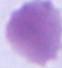

magnification: 1000x
modality: photomicrograph
identification: erythrocyte